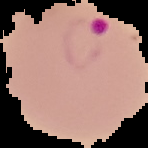

Summary:
  - Image size: 148×148 pixels
  - Malaria status: parasitized
  - Image type: segmented cell region with the area outside set to black
  - Preparation: thin blood film